Locate every Plasmodium malariae-infected red blood cell.
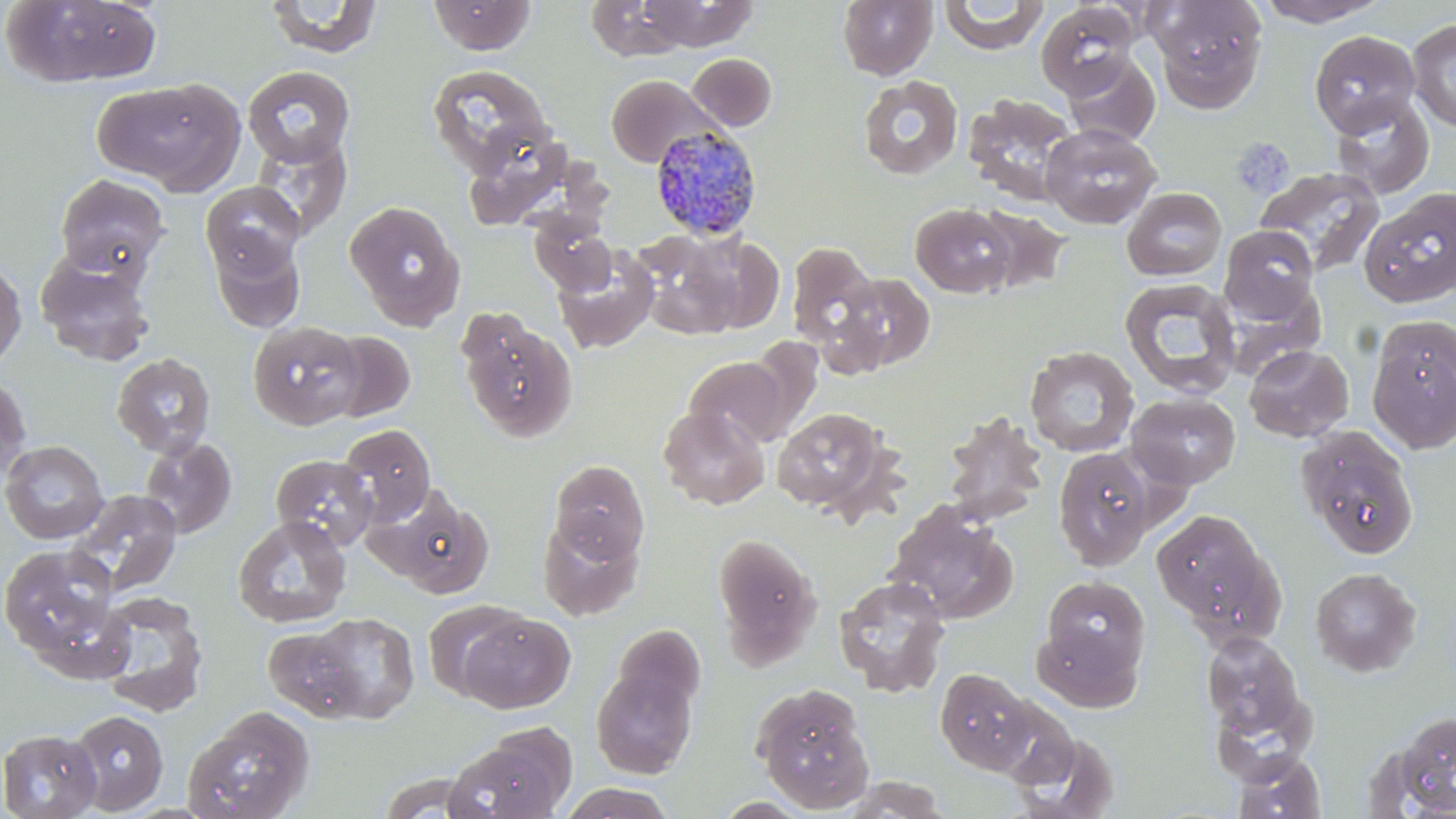

Approximate bounding boxes as (x1, y1, x2, y2) in pixels.
Plasmodium malariae-infected red blood cells: (649, 124, 763, 240).

Platelet locations: (1230, 138, 1294, 199). Uninfected red blood cell locations: (1, 0, 163, 87), (265, 0, 384, 58), (428, 0, 536, 55), (584, 0, 690, 62), (638, 0, 758, 50), (837, 0, 938, 80), (939, 0, 1049, 54), (1147, 0, 1269, 111), (1254, 0, 1391, 27), (1036, 2, 1138, 98), (1407, 18, 1456, 133), (1309, 30, 1420, 137), (1061, 52, 1161, 146), (688, 53, 777, 131), (427, 64, 555, 178), (242, 66, 355, 166), (605, 74, 721, 168), (858, 75, 963, 179), (95, 77, 245, 195), (962, 93, 1081, 206), (1329, 93, 1435, 199), (1040, 123, 1162, 228), (250, 133, 352, 240), (1254, 167, 1384, 278), (53, 173, 171, 278), (202, 182, 305, 285), (1122, 186, 1228, 281), (1359, 188, 1456, 307), (344, 199, 466, 330), (910, 202, 1019, 298), (530, 216, 616, 295), (1218, 225, 1321, 322), (632, 232, 745, 340), (208, 233, 306, 332), (683, 233, 785, 333), (787, 241, 880, 352), (553, 247, 659, 354), (35, 255, 157, 367), (0, 256, 27, 372), (832, 273, 937, 373), (1119, 278, 1242, 399), (456, 309, 578, 443), (1366, 318, 1456, 454), (248, 320, 364, 430), (324, 330, 415, 422), (1243, 344, 1354, 442), (1024, 346, 1140, 458), (112, 353, 216, 458), (683, 355, 789, 448), (0, 371, 33, 485), (1126, 392, 1241, 489), (658, 406, 770, 510), (771, 407, 892, 515), (942, 411, 1048, 527), (337, 424, 436, 526), (1295, 425, 1420, 559), (140, 436, 237, 540), (0, 440, 108, 544), (1053, 447, 1157, 571), (271, 454, 377, 550), (549, 459, 649, 563), (367, 484, 496, 598), (66, 488, 183, 597), (886, 503, 1019, 624), (1151, 508, 1284, 642), (232, 515, 352, 629), (537, 515, 644, 620), (710, 531, 822, 668), (1, 544, 123, 667), (1309, 567, 1422, 678), (834, 574, 951, 697), (1042, 576, 1150, 677), (92, 589, 210, 717), (423, 600, 528, 701), (306, 612, 420, 722), (458, 612, 575, 713), (1033, 622, 1141, 712), (263, 624, 368, 721), (609, 624, 706, 721), (1201, 632, 1307, 743), (590, 666, 698, 778), (935, 668, 1037, 774), (751, 682, 875, 813), (988, 697, 1080, 789), (182, 705, 316, 819), (66, 709, 168, 814), (1388, 710, 1456, 814), (445, 727, 575, 819), (0, 729, 102, 819), (1010, 729, 1120, 816), (1231, 750, 1326, 818), (835, 776, 952, 817), (558, 783, 677, 819). Slide-level diagnosis: Plasmodium malariae. One field of a larger specimen. May-Grünwald-Giemsa-stained preparation. Image is 1456×819 pixels. Optical microscopy. Thin blood film. Captured at 1000x magnification.